Locate every Plasmodium malariae-infected red blood cell.
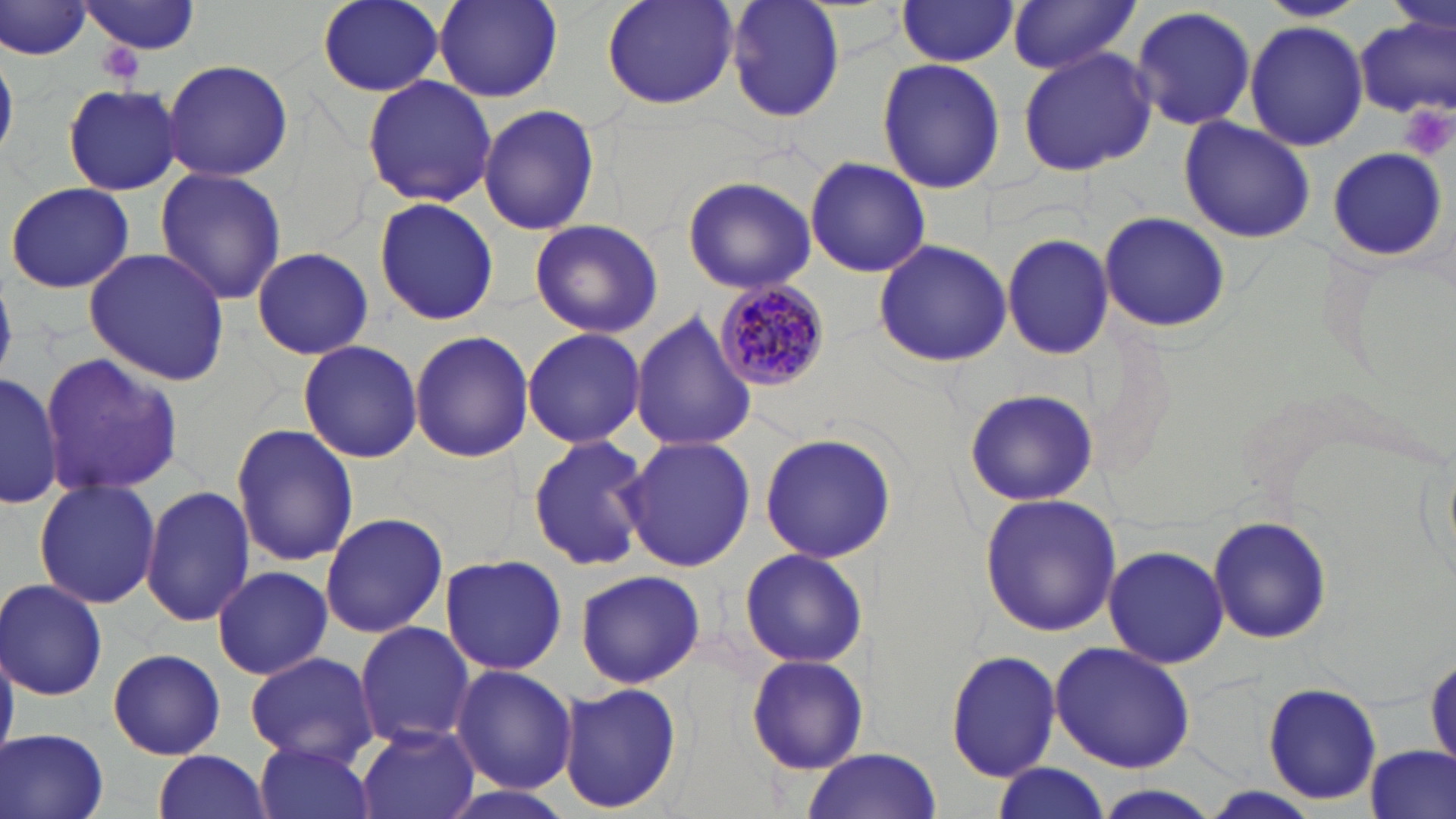
Approximate bounding boxes as (x1, y1, x2, y2) in pixels.
Plasmodium malariae-infected red blood cells: (714, 278, 832, 393).

Summary:
  - Uninfected red blood cell locations: (316, 0, 446, 95), (434, 0, 563, 102), (599, 0, 739, 110), (727, 0, 847, 122), (1257, 0, 1367, 23), (78, 1, 199, 56), (893, 1, 1020, 66), (1007, 1, 1140, 75), (1, 3, 95, 62), (1131, 5, 1258, 134), (1354, 14, 1455, 120), (1244, 20, 1368, 151), (0, 47, 17, 161), (1018, 48, 1154, 175), (160, 58, 294, 181), (875, 58, 1006, 194), (360, 74, 497, 209), (62, 85, 183, 196), (478, 101, 601, 237), (1177, 117, 1317, 244), (1325, 145, 1449, 264), (805, 156, 930, 277), (155, 168, 288, 306), (681, 175, 816, 295), (5, 181, 136, 294), (372, 197, 500, 325), (1100, 212, 1233, 333), (528, 217, 663, 338), (1002, 232, 1115, 360), (872, 238, 1012, 369), (83, 246, 230, 384), (252, 247, 373, 357), (631, 311, 757, 453), (523, 326, 647, 449), (409, 330, 534, 464), (296, 340, 422, 464), (37, 351, 185, 497), (0, 370, 65, 510), (961, 388, 1097, 506), (231, 423, 360, 566), (757, 430, 898, 565), (526, 433, 654, 573), (619, 436, 756, 572), (32, 479, 161, 610), (141, 485, 255, 626), (978, 492, 1124, 637), (320, 511, 447, 639), (1206, 514, 1336, 649), (1103, 543, 1230, 668), (738, 547, 870, 669), (438, 554, 569, 675), (211, 564, 333, 679), (573, 570, 705, 687), (1, 579, 109, 701), (354, 621, 475, 748), (1049, 642, 1196, 774), (105, 648, 230, 760), (945, 648, 1061, 783), (745, 652, 869, 774), (245, 653, 378, 767), (451, 665, 577, 794), (557, 680, 681, 814), (1262, 682, 1386, 804), (357, 726, 481, 819), (1, 729, 110, 819), (253, 739, 377, 819), (1361, 747, 1453, 819), (799, 749, 945, 819), (151, 750, 272, 819), (989, 763, 1112, 819), (433, 783, 580, 819)
  - Platelet locations: (1401, 101, 1454, 161)
  - Slide-level diagnosis: Plasmodium malariae
  - Image size: 1456×819 pixels
  - Modality: optical microscopy
  - Field of view: one of a larger specimen
  - Preparation: thin blood film
  - Stain: May-Grünwald-Giemsa
  - Magnification: 1000x